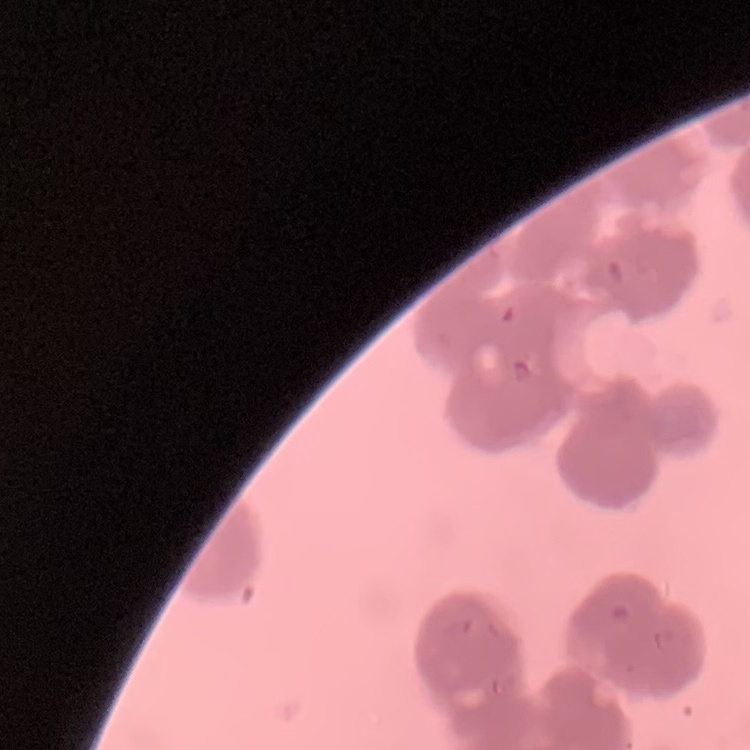

Summary:
  - Erythrocyte morphology: rouleaux formation
  - Image type: square crop of a larger photomicrograph
  - Stain: Field's or Giemsa
  - Preparation: thin blood smear